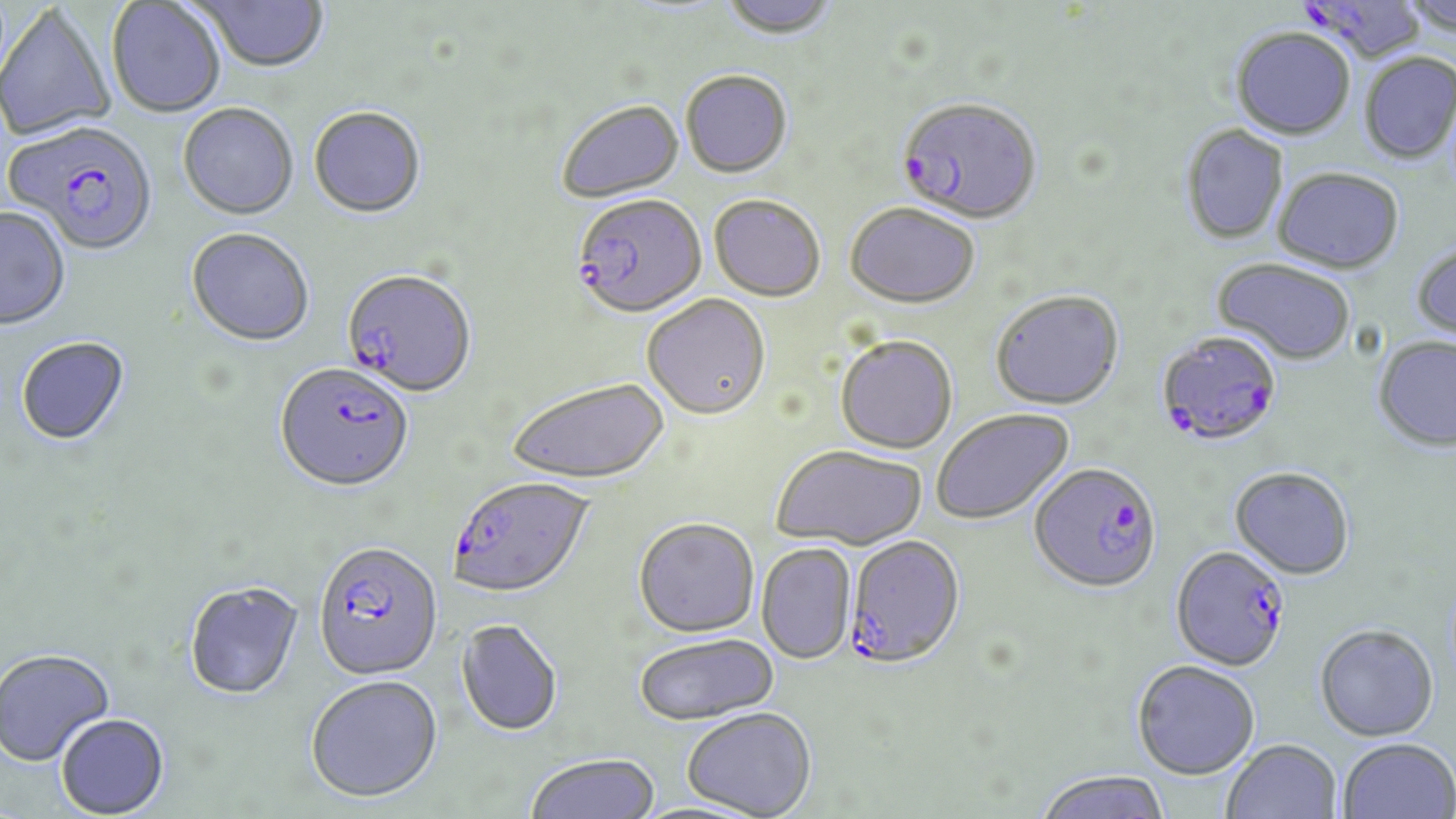
Approximate bounding boxes as [x1, y1, x2, y2] in pixels. Plasmodium falciparum-infected red blood cell locations: [1298, 0, 1425, 68], [897, 97, 1043, 226], [5, 122, 159, 257], [572, 197, 707, 321], [342, 270, 476, 399], [1156, 331, 1283, 448], [275, 362, 415, 494], [1029, 462, 1163, 592], [448, 476, 594, 597], [845, 535, 966, 668], [313, 540, 443, 680], [1171, 544, 1291, 671]. Uninfected red blood cell locations: [193, 0, 330, 75], [717, 0, 840, 41], [1397, 0, 1456, 36], [106, 1, 226, 118], [0, 4, 116, 143], [1230, 27, 1355, 140], [1359, 52, 1456, 163], [680, 70, 793, 179], [556, 100, 684, 204], [178, 104, 298, 220], [308, 107, 427, 220], [1180, 124, 1289, 245], [1273, 167, 1404, 273], [708, 196, 825, 302], [845, 203, 980, 309], [0, 208, 71, 332], [186, 229, 315, 348], [1410, 243, 1456, 344], [1211, 259, 1355, 365], [990, 289, 1124, 409], [642, 295, 771, 422], [835, 334, 958, 454], [1373, 336, 1456, 453], [15, 337, 132, 448], [507, 377, 670, 485], [931, 408, 1074, 524], [771, 444, 927, 549], [1230, 466, 1355, 579], [633, 517, 759, 637], [756, 543, 856, 664], [185, 581, 304, 700], [456, 618, 564, 736], [1315, 623, 1439, 741], [633, 632, 778, 725], [0, 650, 115, 768], [1132, 660, 1260, 779], [305, 675, 443, 802], [681, 707, 817, 818], [56, 715, 170, 818], [1338, 738, 1456, 819], [1221, 739, 1342, 819], [525, 753, 659, 819], [1035, 769, 1171, 819]. Slide-level diagnosis: Plasmodium falciparum. Thin blood smear. Single field of view. Captured at 1000x magnification. Light microscopy. Image is 1456×819 pixels. May-Grünwald-Giemsa stain.